Classify this cell by malaria status.
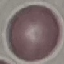
It is uninfected.

Giemsa-stained preparation. Acquired by smartphone through the microscope eyepiece. Cell patch, automatically extracted from a larger field of view and resized to 64 × 64 pixels. Thin blood film.